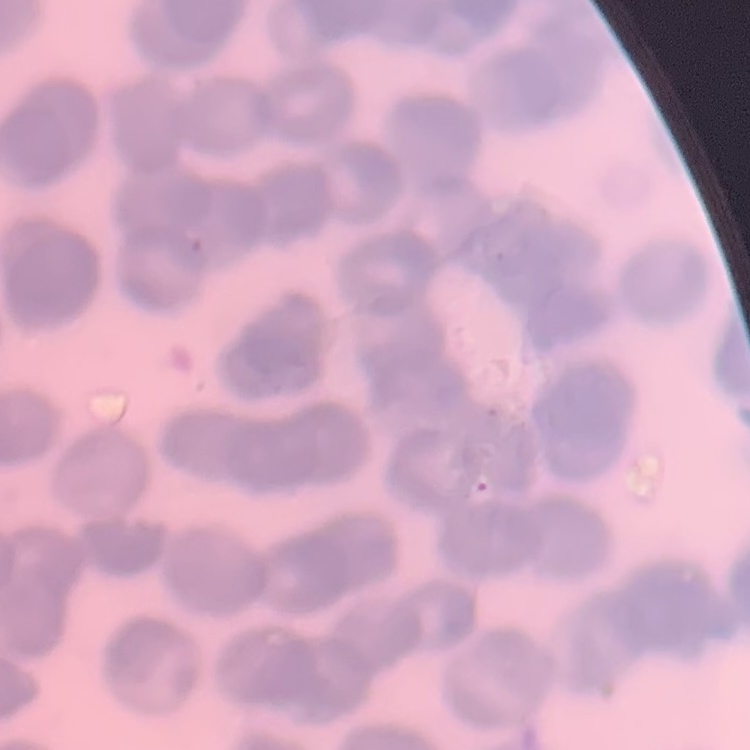
Summary:
  - Erythrocyte morphology: rouleaux formation
  - Image type: square crop of a larger photomicrograph
  - Stain: Field's or Giemsa
  - Preparation: thin peripheral smear